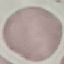

{
  "result": "negative for malaria parasites",
  "stain": "Giemsa",
  "capture": "smartphone camera at the microscope eyepiece",
  "image_type": "cell patch, automatically extracted from a larger field of view and resized to 64 × 64 pixels",
  "preparation": "thin blood smear"
}